Identify the parasite.
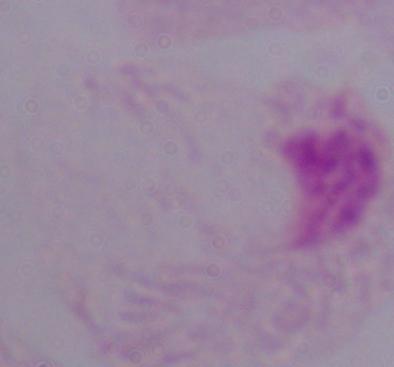
This is a trichomonad.

Micrograph. Captured at 1000x magnification.